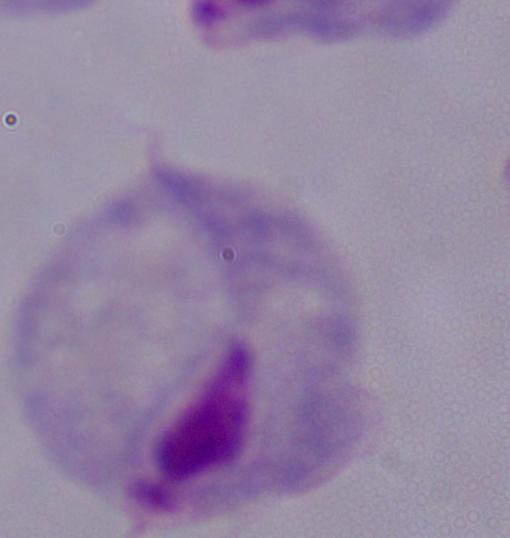 Captured at 1000x magnification. A trichomonad is shown. Micrograph.